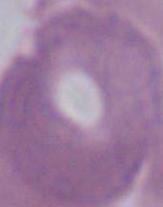

Summary:
  - Magnification: 1000x
  - Modality: micrograph
  - Identification: erythrocyte